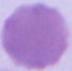

modality = photomicrograph
identification = red blood cell
magnification = 1000x